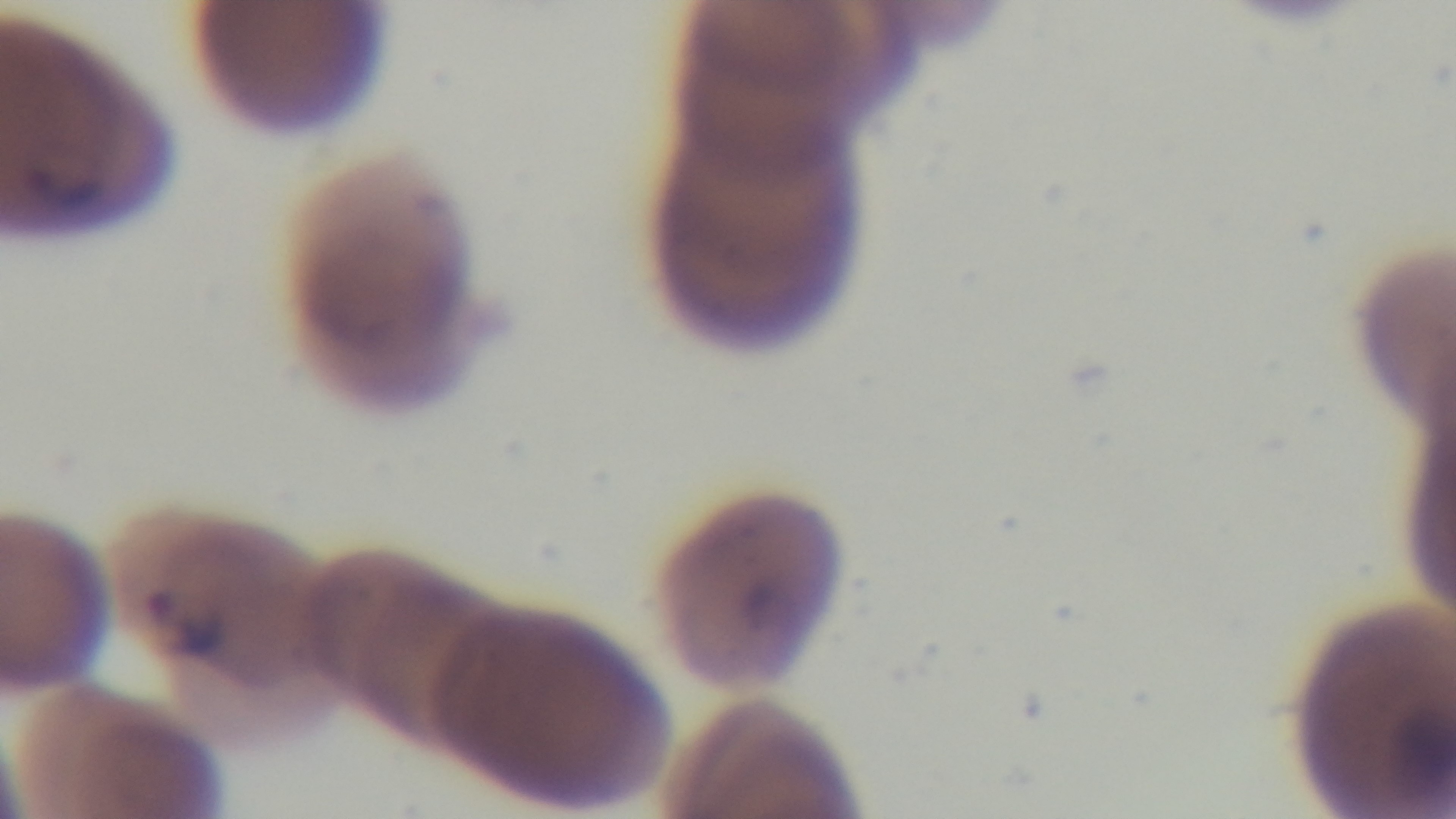

Summary:
  - Field of view: single
  - Capture: mounted 4K digital camera
  - Stain: Giemsa
  - Preparation: thin
  - Malaria status: infected
  - Objective: 100x oil immersion
  - Modality: light microscopy